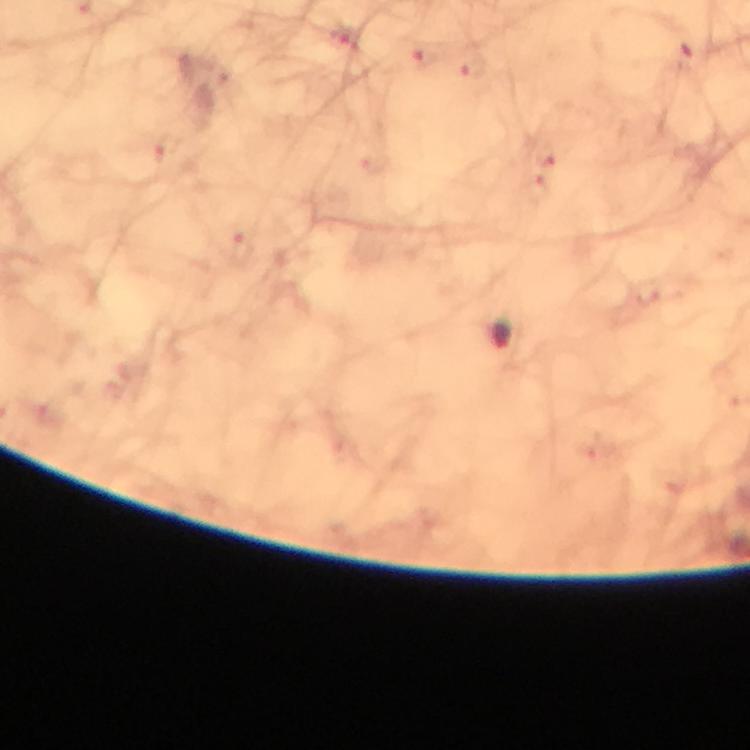

Approximate centers as [x, y] in pixels. Malaria parasite locations: [501, 334]. Thick blood smear. From a diagnostic examination for malaria. At 100x magnification. Giemsa-stained preparation. Immersion oil applied. Photographed through the microscope with a smartphone camera. Image is 750×750 pixels. Cropped region of a single field of view.